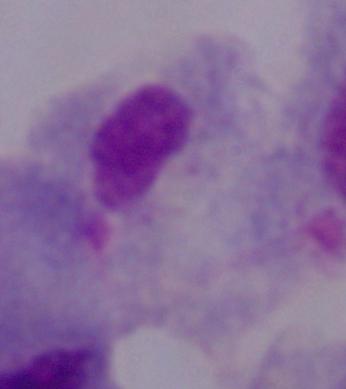

Summary:
  - Modality: photomicrograph
  - Identification: trichomonad
  - Magnification: 1000x